Name the cell type shown.
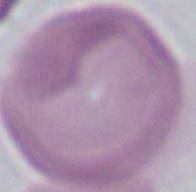

This is an erythrocyte.

{
  "modality": "photomicrograph",
  "magnification": "1000x"
}